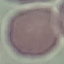

Summary:
  - Result: no malaria parasites seen
  - Preparation: thin blood film
  - Capture: smartphone camera at the microscope eyepiece
  - Stain: Giemsa
  - Image type: automatically extracted cell patch, resized to 64 × 64 pixels